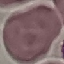
Result: no malaria parasites seen. Giemsa stain. Acquired by smartphone through the microscope eyepiece. Cell patch, automatically extracted from a larger field of view and resized to 64 × 64 pixels. Thin blood film.